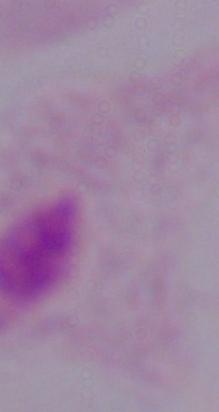
magnification = 1000x
identification = trichomonad
modality = micrograph